Outline each blood parasite and name the species.
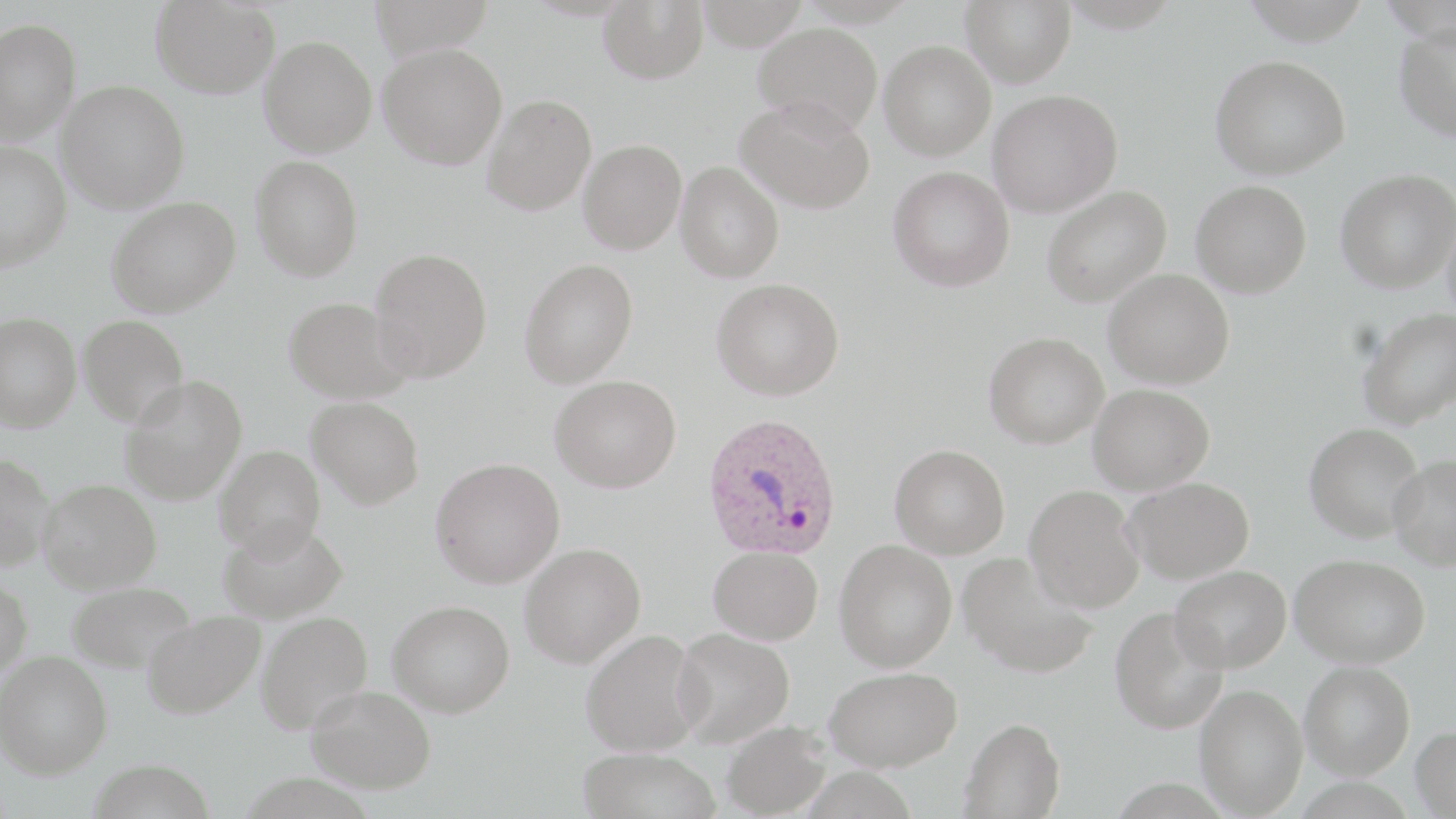
Approximate bounding boxes as named x1/y1/x2/y2 corners in pixels.
Plasmodium ovale-infected red blood cells: (x1=702, y1=411, x2=843, y2=562).
No Plasmodium falciparum, Plasmodium malariae, Plasmodium vivax, Babesia divergens, or Trypanosoma brucei observed.

{
  "slide_level_diagnosis": "Plasmodium ovale",
  "field_of_view": "single",
  "modality": "light microscopy",
  "stain": "May-Grünwald-Giemsa",
  "magnification": "1000x",
  "preparation": "thin blood film",
  "image_size": "1456×819 pixels",
  "uninfected_red_blood_cell_locations": "approximate bounding boxes as named x1/y1/x2/y2 corners in pixels: (x1=367, y1=0, x2=496, y2=57), (x1=598, y1=0, x2=708, y2=83), (x1=695, y1=0, x2=810, y2=51), (x1=960, y1=0, x2=1076, y2=87), (x1=151, y1=1, x2=280, y2=99), (x1=0, y1=17, x2=81, y2=144), (x1=753, y1=22, x2=883, y2=134), (x1=1394, y1=23, x2=1456, y2=141), (x1=259, y1=36, x2=377, y2=157), (x1=879, y1=40, x2=996, y2=161), (x1=378, y1=43, x2=507, y2=169), (x1=1210, y1=55, x2=1350, y2=180), (x1=57, y1=80, x2=190, y2=213), (x1=988, y1=89, x2=1122, y2=217), (x1=481, y1=94, x2=596, y2=215), (x1=736, y1=97, x2=875, y2=214), (x1=579, y1=139, x2=686, y2=254), (x1=0, y1=140, x2=72, y2=270), (x1=251, y1=155, x2=363, y2=281), (x1=674, y1=161, x2=785, y2=282), (x1=887, y1=165, x2=1015, y2=292), (x1=1336, y1=169, x2=1456, y2=293), (x1=1191, y1=180, x2=1312, y2=298), (x1=1042, y1=185, x2=1171, y2=308), (x1=107, y1=196, x2=241, y2=316), (x1=1443, y1=214, x2=1456, y2=323), (x1=370, y1=248, x2=493, y2=381), (x1=519, y1=257, x2=639, y2=388), (x1=1103, y1=268, x2=1234, y2=389), (x1=712, y1=278, x2=845, y2=401), (x1=284, y1=296, x2=411, y2=403), (x1=1357, y1=307, x2=1456, y2=429), (x1=0, y1=312, x2=82, y2=431), (x1=78, y1=315, x2=189, y2=426), (x1=983, y1=331, x2=1109, y2=448), (x1=550, y1=374, x2=681, y2=492), (x1=118, y1=376, x2=248, y2=503), (x1=1088, y1=383, x2=1214, y2=495), (x1=307, y1=396, x2=425, y2=509), (x1=1305, y1=422, x2=1424, y2=542), (x1=890, y1=444, x2=1010, y2=559), (x1=214, y1=445, x2=325, y2=558), (x1=0, y1=452, x2=53, y2=570), (x1=1389, y1=455, x2=1456, y2=571), (x1=430, y1=458, x2=565, y2=588), (x1=1123, y1=476, x2=1255, y2=583), (x1=38, y1=479, x2=161, y2=593), (x1=1025, y1=483, x2=1145, y2=613), (x1=218, y1=519, x2=348, y2=623), (x1=834, y1=539, x2=957, y2=672), (x1=519, y1=542, x2=646, y2=668), (x1=708, y1=545, x2=823, y2=645), (x1=958, y1=551, x2=1097, y2=678), (x1=1291, y1=553, x2=1430, y2=667), (x1=1170, y1=565, x2=1291, y2=672), (x1=0, y1=575, x2=33, y2=682), (x1=67, y1=581, x2=196, y2=673), (x1=388, y1=600, x2=514, y2=717), (x1=1110, y1=605, x2=1228, y2=734), (x1=142, y1=610, x2=265, y2=719), (x1=255, y1=611, x2=373, y2=734), (x1=672, y1=627, x2=796, y2=747), (x1=580, y1=628, x2=705, y2=756), (x1=0, y1=650, x2=112, y2=779), (x1=1300, y1=661, x2=1415, y2=780), (x1=825, y1=666, x2=962, y2=771), (x1=1194, y1=683, x2=1307, y2=816), (x1=306, y1=684, x2=436, y2=793), (x1=959, y1=717, x2=1066, y2=818), (x1=721, y1=720, x2=831, y2=818), (x1=1411, y1=725, x2=1456, y2=817), (x1=577, y1=748, x2=721, y2=819), (x1=89, y1=759, x2=216, y2=819)"
}